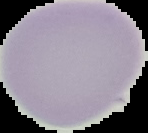

image size = 148×133 pixels
image type = cell region segmented out of the field of view; surrounding area masked to black
malaria status = uninfected
preparation = thin blood smear